Outline each Trypanosoma brucei.
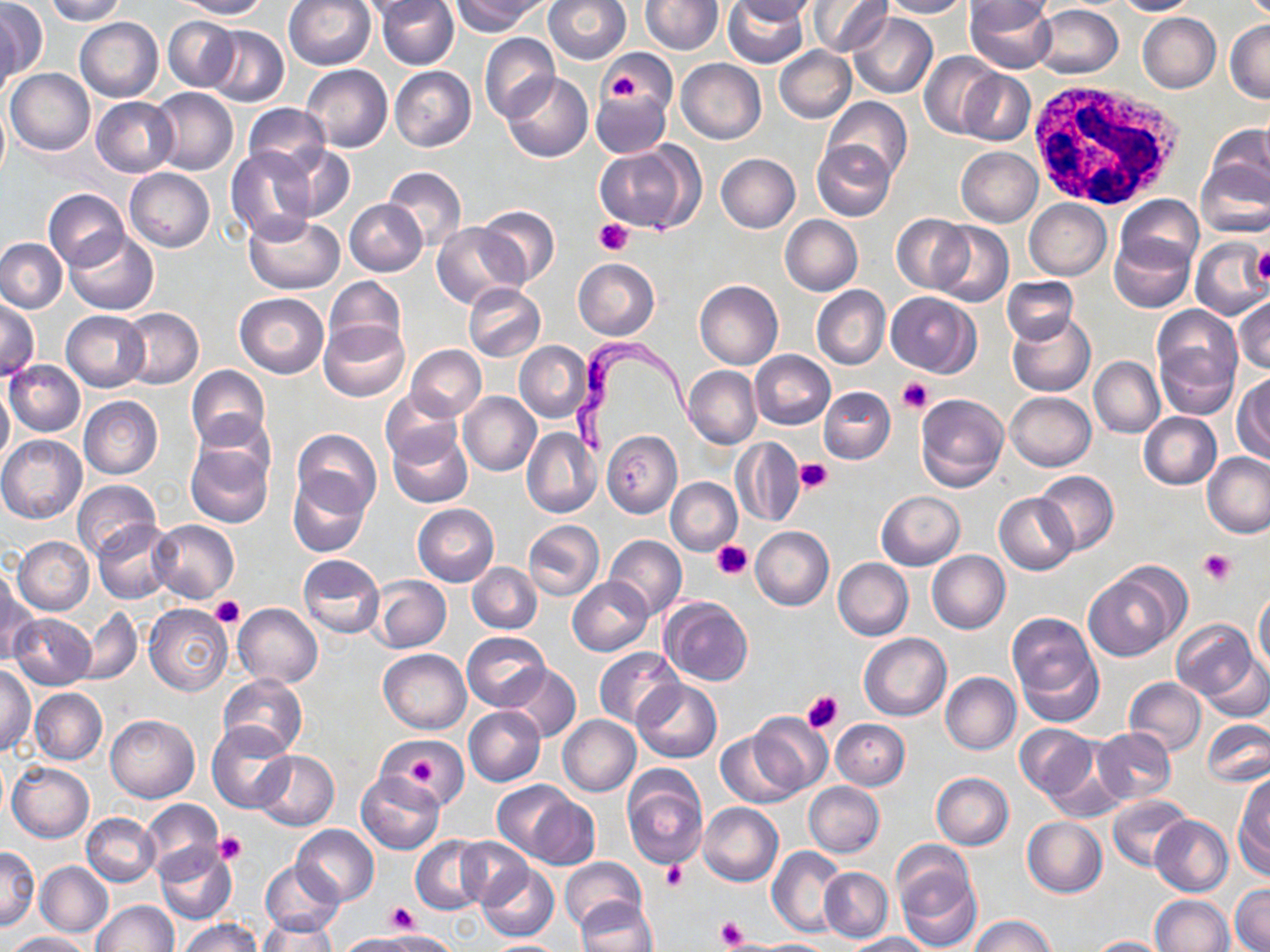

Approximate bounding boxes as (x1, y1, x2, y2) in pixels.
Trypanosoma brucei: (566, 336, 702, 456).

Summary:
  - Platelet locations: (602, 65, 645, 104), (595, 219, 633, 255), (1249, 249, 1270, 287), (899, 377, 932, 413), (796, 457, 832, 495), (711, 543, 751, 581), (1200, 550, 1234, 585), (208, 596, 244, 629), (801, 688, 845, 732), (409, 756, 437, 785), (214, 832, 247, 865), (661, 862, 688, 889), (384, 901, 417, 933), (716, 917, 746, 951)
  - Uninfected red blood cell locations: (0, 0, 44, 85), (44, 0, 125, 24), (177, 0, 269, 20), (283, 0, 375, 71), (358, 0, 445, 20), (377, 0, 458, 70), (452, 0, 543, 36), (545, 0, 630, 63), (640, 0, 722, 55), (725, 0, 807, 67), (731, 0, 815, 22), (807, 0, 892, 57), (880, 0, 971, 18), (1113, 0, 1195, 16), (966, 1, 1057, 71), (966, 2, 1054, 34), (1030, 5, 1122, 79), (0, 9, 20, 102), (848, 13, 938, 99), (1137, 13, 1220, 92), (74, 17, 163, 101), (163, 17, 240, 90), (1225, 20, 1270, 103), (204, 26, 288, 108), (480, 34, 559, 122), (774, 45, 856, 122), (600, 48, 679, 117), (919, 51, 1002, 137), (676, 59, 766, 143), (301, 64, 392, 152), (390, 66, 476, 151), (5, 69, 94, 154), (958, 70, 1035, 145), (502, 72, 593, 162), (150, 87, 239, 176), (592, 89, 671, 158), (0, 96, 10, 188), (92, 96, 179, 176), (823, 97, 912, 184), (244, 103, 330, 177), (1204, 124, 1270, 205), (812, 140, 895, 221), (595, 144, 699, 232), (275, 145, 356, 221), (956, 146, 1042, 227), (225, 147, 320, 246), (716, 153, 800, 232), (1196, 157, 1270, 239), (383, 166, 467, 250), (125, 168, 215, 252), (43, 188, 130, 270), (1114, 196, 1203, 274), (345, 199, 426, 276), (1025, 199, 1112, 279), (476, 205, 560, 287), (243, 212, 345, 293), (892, 215, 973, 293), (780, 216, 862, 296), (431, 221, 523, 308), (931, 221, 1013, 308), (64, 230, 158, 313), (1109, 237, 1194, 312), (0, 238, 67, 312), (1190, 238, 1269, 320), (573, 258, 659, 340), (324, 276, 406, 357), (1002, 276, 1079, 344), (695, 280, 783, 369), (463, 283, 545, 361), (812, 286, 890, 369), (885, 291, 980, 376), (235, 293, 328, 378), (1233, 297, 1270, 374), (0, 298, 39, 380), (119, 309, 203, 388), (1151, 309, 1241, 415), (62, 311, 150, 392), (1007, 313, 1095, 397), (318, 319, 410, 402), (515, 342, 591, 421), (407, 345, 486, 419), (750, 351, 835, 429), (1089, 356, 1164, 438), (4, 360, 85, 437), (185, 365, 270, 451), (683, 366, 762, 449), (1233, 373, 1270, 463), (0, 382, 13, 467), (819, 386, 895, 464), (380, 388, 464, 469), (458, 391, 541, 476), (1005, 392, 1096, 471), (915, 394, 1009, 493), (79, 396, 163, 479), (189, 410, 277, 494), (1139, 411, 1221, 489), (387, 426, 473, 508), (521, 426, 601, 519), (291, 429, 381, 516), (601, 431, 681, 516), (0, 435, 87, 523), (731, 438, 805, 527), (184, 439, 274, 528), (1202, 452, 1270, 537), (1034, 469, 1118, 555), (288, 470, 371, 558), (666, 478, 741, 555), (72, 480, 161, 560), (876, 491, 965, 570), (995, 492, 1078, 574), (412, 504, 499, 586), (149, 519, 240, 602), (523, 519, 603, 601), (93, 520, 179, 604), (750, 526, 833, 610), (605, 535, 686, 619), (13, 536, 93, 615), (927, 551, 1010, 634), (297, 554, 385, 638), (833, 558, 912, 641), (467, 562, 542, 634), (1084, 565, 1186, 660), (371, 575, 451, 653), (567, 577, 653, 655), (1, 578, 37, 668), (1254, 588, 1270, 677), (661, 597, 752, 686), (233, 603, 323, 688), (145, 604, 232, 695), (75, 606, 143, 686), (9, 612, 96, 690), (1006, 612, 1102, 723), (1171, 620, 1258, 700), (463, 631, 551, 711), (859, 633, 951, 721), (381, 642, 548, 720), (594, 647, 684, 728), (378, 649, 471, 734), (1203, 656, 1270, 723), (501, 663, 582, 742), (0, 666, 35, 755), (940, 672, 1020, 754), (217, 673, 307, 757), (1124, 677, 1206, 756), (632, 680, 721, 763), (30, 688, 107, 764), (464, 706, 545, 787), (748, 711, 833, 796), (105, 713, 200, 802), (557, 716, 641, 796), (1201, 718, 1270, 788), (830, 719, 909, 790), (208, 721, 297, 813), (1014, 724, 1096, 799), (1091, 726, 1177, 805), (716, 731, 802, 807), (383, 737, 465, 807), (253, 749, 339, 830), (1041, 753, 1130, 823), (8, 762, 94, 842), (622, 769, 708, 870), (357, 772, 445, 853), (931, 772, 1014, 849), (1236, 776, 1270, 871), (493, 780, 583, 861), (805, 781, 884, 856), (1107, 794, 1191, 871), (524, 795, 597, 869), (139, 799, 224, 883), (698, 803, 783, 886), (81, 813, 160, 886), (1151, 815, 1233, 895), (1022, 816, 1107, 897), (293, 824, 379, 904), (411, 836, 488, 914), (456, 837, 530, 906), (154, 842, 236, 925), (0, 846, 40, 929), (767, 846, 847, 938), (894, 854, 981, 952), (560, 858, 648, 932), (261, 859, 344, 938), (35, 861, 113, 937), (477, 863, 560, 942), (819, 867, 892, 942), (1230, 885, 1269, 952), (1150, 895, 1234, 952), (574, 898, 657, 952), (92, 900, 177, 951), (970, 915, 1055, 952), (179, 918, 262, 952), (261, 918, 337, 952), (6, 931, 89, 951), (365, 932, 452, 952), (848, 932, 933, 951), (1087, 935, 1172, 952), (481, 940, 566, 951), (750, 940, 835, 951)
  - White blood cell locations: (1023, 78, 1191, 213)
  - Slide-level diagnosis: Trypanosoma brucei
  - Magnification: 1000x
  - Preparation: thin blood smear
  - Modality: optical microscopy
  - Field of view: one of a larger specimen
  - Stain: May-Grünwald-Giemsa
  - Image size: 1270×952 pixels